Give the preparation type.
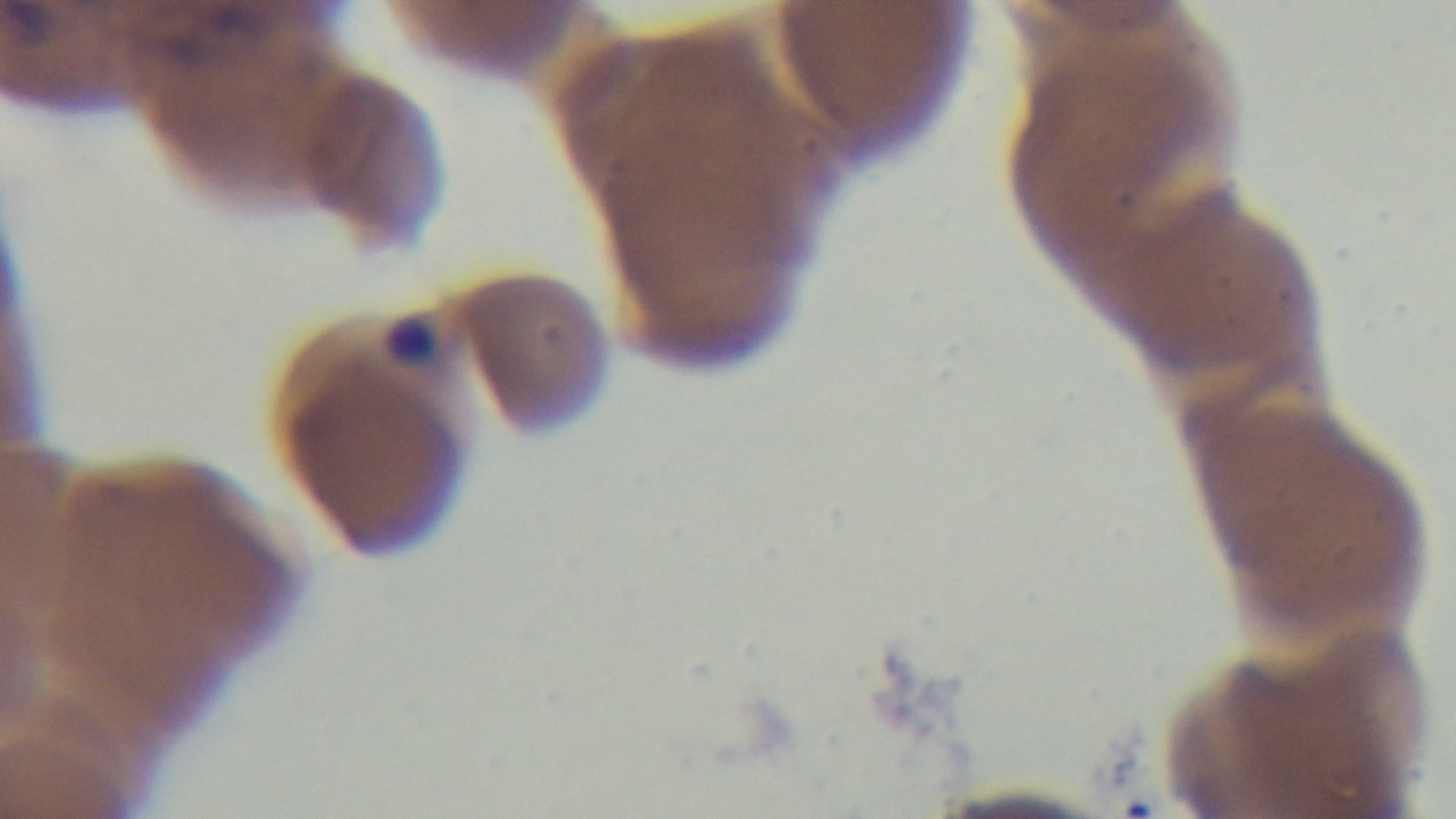

It is a thin blood film.

Summary:
  - Malaria status: positive
  - Stain: Giemsa
  - Modality: light microscopy
  - Objective: 100x oil immersion
  - Field of view: one from the slide
  - Capture: mounted 4K digital camera